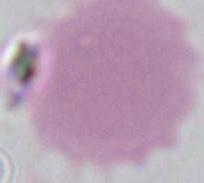
modality: photomicrograph
magnification: 1000x
identification: red blood cell